State the blood parasite species.
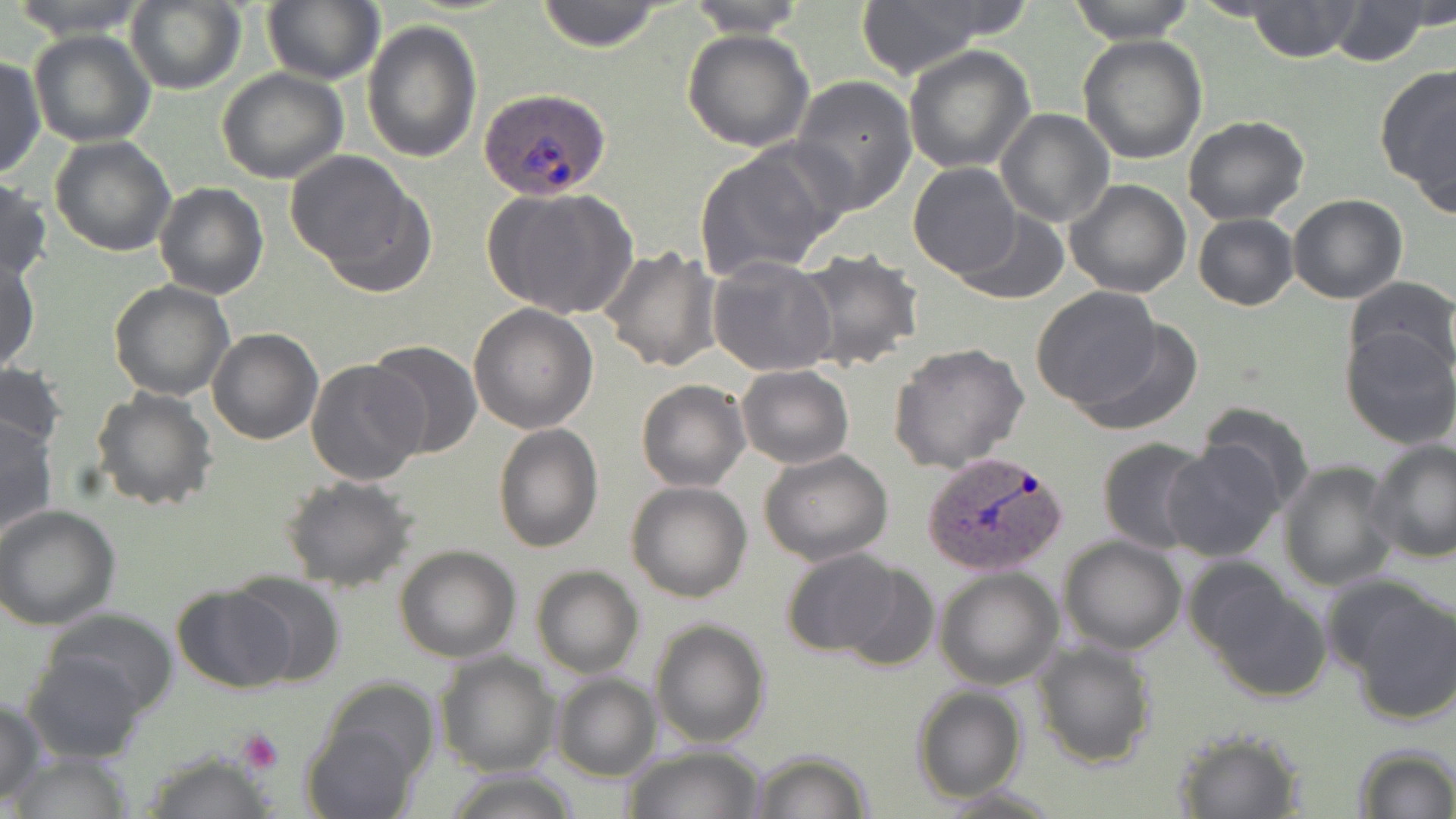
Plasmodium ovale.

image size = 1456×819 pixels
Plasmodium ovale-infected red blood cell locations = approximate bounding boxes as (x1,y1)-(x2,y2) corner pairs in pixels: (480,88)-(612,202), (923,450)-(1070,575)
stain = May-Grünwald-Giemsa
magnification = 1000x
preparation = thin blood smear
field of view = one of a larger specimen
uninfected red blood cell locations = approximate bounding boxes as (x1,y1)-(x2,y2) corner pairs in pixels: (9,0)-(152,40), (261,0)-(384,86), (535,0)-(667,52), (681,0)-(813,37), (1065,0)-(1198,43), (1247,0)-(1362,62), (125,1)-(246,93), (1325,2)-(1436,66), (855,4)-(990,80), (362,19)-(483,163), (683,28)-(815,151), (30,30)-(154,147), (1078,33)-(1207,165), (905,43)-(1036,173), (0,55)-(45,179), (1375,62)-(1456,205), (216,68)-(348,183), (790,74)-(918,217), (995,109)-(1114,228), (1183,115)-(1309,224), (49,136)-(177,257), (693,142)-(841,280), (285,151)-(433,294), (907,163)-(1023,279), (0,177)-(50,285), (1064,179)-(1191,298), (154,182)-(268,299), (486,187)-(635,321), (1288,194)-(1408,304), (951,209)-(1068,306), (1192,212)-(1297,311), (600,246)-(723,373), (796,249)-(922,371), (1,256)-(39,375), (708,256)-(839,376), (1345,275)-(1455,380), (109,281)-(234,402), (1030,285)-(1165,412), (468,303)-(600,433), (1072,318)-(1203,437), (206,328)-(322,445), (1340,328)-(1456,449), (368,342)-(481,458), (889,343)-(1029,473), (0,360)-(66,457), (306,360)-(428,486), (735,364)-(854,469), (637,380)-(750,491), (91,386)-(218,513), (1197,401)-(1315,512), (0,417)-(58,540), (495,423)-(603,552), (1096,437)-(1213,553), (1366,438)-(1456,563), (1161,441)-(1284,562), (759,450)-(895,565), (1279,461)-(1397,592), (282,474)-(418,591), (626,480)-(752,603), (0,504)-(122,629), (1058,535)-(1187,656), (393,545)-(521,663), (778,548)-(907,660), (828,562)-(942,672), (531,565)-(643,679), (934,567)-(1063,690), (227,573)-(345,688), (1196,578)-(1332,703), (172,585)-(296,693), (1346,586)-(1456,727), (43,609)-(180,715), (649,619)-(771,748), (1031,638)-(1157,769), (22,650)-(149,765), (435,651)-(559,776), (551,674)-(660,782), (320,678)-(439,786), (911,685)-(1028,803), (0,696)-(47,804), (300,720)-(420,819), (1170,726)-(1307,818), (621,743)-(767,819), (1352,743)-(1456,819), (135,748)-(276,817), (8,750)-(136,819), (749,750)-(873,819), (445,769)-(580,819), (931,785)-(1068,817)
platelet locations = approximate bounding boxes as (x1,y1)-(x2,y2) corner pairs in pixels: (237,730)-(284,775)
modality = light microscopy